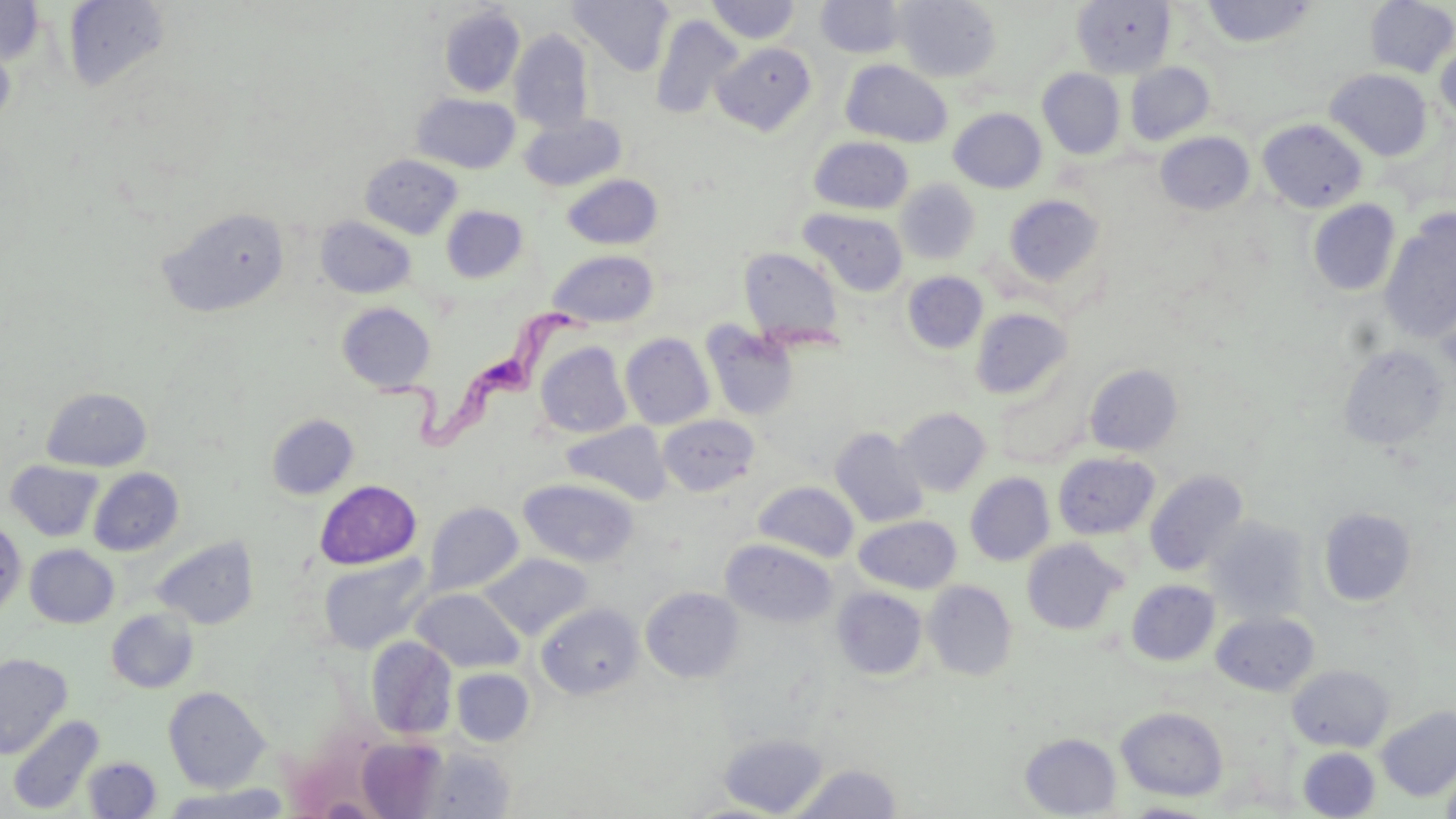
slide-level diagnosis = Trypanosoma brucei
uninfected red blood cell locations = approximate bounding boxes as named x1/y1/x2/y2 corners in pixels: (x1=0, y1=0, x2=46, y2=64), (x1=569, y1=0, x2=673, y2=76), (x1=893, y1=0, x2=1001, y2=82), (x1=1073, y1=0, x2=1175, y2=78), (x1=1202, y1=0, x2=1317, y2=47), (x1=1364, y1=0, x2=1456, y2=77), (x1=63, y1=1, x2=171, y2=93), (x1=705, y1=1, x2=802, y2=44), (x1=816, y1=1, x2=908, y2=59), (x1=439, y1=5, x2=525, y2=97), (x1=651, y1=14, x2=743, y2=121), (x1=0, y1=28, x2=17, y2=134), (x1=509, y1=29, x2=595, y2=134), (x1=1434, y1=38, x2=1456, y2=130), (x1=711, y1=42, x2=817, y2=135), (x1=841, y1=60, x2=953, y2=148), (x1=1125, y1=62, x2=1215, y2=146), (x1=1037, y1=68, x2=1125, y2=159), (x1=1325, y1=68, x2=1432, y2=160), (x1=411, y1=93, x2=520, y2=174), (x1=949, y1=108, x2=1047, y2=193), (x1=520, y1=113, x2=627, y2=192), (x1=1257, y1=118, x2=1368, y2=213), (x1=1155, y1=132, x2=1255, y2=216), (x1=809, y1=136, x2=913, y2=215), (x1=361, y1=154, x2=462, y2=238), (x1=561, y1=174, x2=662, y2=250), (x1=895, y1=179, x2=980, y2=264), (x1=1003, y1=194, x2=1105, y2=288), (x1=1306, y1=199, x2=1401, y2=298), (x1=441, y1=205, x2=529, y2=283), (x1=159, y1=207, x2=291, y2=318), (x1=799, y1=208, x2=908, y2=297), (x1=1379, y1=212, x2=1456, y2=345), (x1=316, y1=216, x2=416, y2=298), (x1=739, y1=247, x2=844, y2=347), (x1=548, y1=250, x2=659, y2=328), (x1=902, y1=271, x2=988, y2=354), (x1=1433, y1=284, x2=1456, y2=377), (x1=337, y1=302, x2=436, y2=393), (x1=970, y1=307, x2=1073, y2=400), (x1=700, y1=321, x2=799, y2=421), (x1=620, y1=333, x2=715, y2=429), (x1=535, y1=341, x2=633, y2=439), (x1=1337, y1=345, x2=1451, y2=451), (x1=1085, y1=364, x2=1183, y2=456), (x1=992, y1=378, x2=1091, y2=469), (x1=41, y1=387, x2=152, y2=472), (x1=896, y1=407, x2=991, y2=496), (x1=266, y1=413, x2=359, y2=499), (x1=658, y1=414, x2=761, y2=497), (x1=562, y1=421, x2=672, y2=504), (x1=830, y1=427, x2=929, y2=527), (x1=1053, y1=453, x2=1160, y2=540), (x1=6, y1=460, x2=104, y2=542), (x1=88, y1=467, x2=184, y2=557), (x1=1145, y1=469, x2=1249, y2=577), (x1=965, y1=473, x2=1055, y2=566), (x1=519, y1=478, x2=638, y2=567), (x1=315, y1=480, x2=421, y2=569), (x1=753, y1=481, x2=859, y2=562), (x1=423, y1=502, x2=524, y2=596), (x1=1318, y1=507, x2=1417, y2=607), (x1=853, y1=515, x2=962, y2=593), (x1=1205, y1=515, x2=1312, y2=623), (x1=0, y1=521, x2=27, y2=616), (x1=151, y1=536, x2=259, y2=630), (x1=1021, y1=538, x2=1127, y2=635), (x1=721, y1=539, x2=837, y2=628), (x1=25, y1=544, x2=119, y2=628), (x1=480, y1=553, x2=592, y2=639), (x1=319, y1=554, x2=431, y2=654), (x1=923, y1=580, x2=1017, y2=681), (x1=1126, y1=580, x2=1220, y2=666), (x1=640, y1=586, x2=745, y2=682), (x1=411, y1=587, x2=524, y2=673), (x1=832, y1=587, x2=928, y2=680), (x1=536, y1=601, x2=644, y2=699), (x1=106, y1=608, x2=199, y2=693), (x1=1211, y1=611, x2=1319, y2=695), (x1=365, y1=636, x2=458, y2=739), (x1=0, y1=653, x2=72, y2=759), (x1=1287, y1=665, x2=1394, y2=751), (x1=451, y1=668, x2=534, y2=745), (x1=163, y1=686, x2=270, y2=792), (x1=1376, y1=706, x2=1456, y2=801), (x1=1117, y1=707, x2=1229, y2=801), (x1=7, y1=714, x2=104, y2=815), (x1=719, y1=732, x2=828, y2=817), (x1=1020, y1=733, x2=1122, y2=818), (x1=357, y1=736, x2=448, y2=818), (x1=1298, y1=747, x2=1381, y2=818), (x1=1441, y1=755, x2=1456, y2=819), (x1=83, y1=757, x2=161, y2=818), (x1=791, y1=762, x2=902, y2=819), (x1=156, y1=783, x2=292, y2=819), (x1=1120, y1=801, x2=1220, y2=818)
stain = May-Grünwald-Giemsa
modality = optical microscopy
field of view = single
Trypanosoma brucei locations = approximate bounding boxes as named x1/y1/x2/y2 corners in pixels: (x1=374, y1=304, x2=594, y2=451)
image size = 1456×819 pixels
preparation = thin blood smear
magnification = 1000x